Locate every leukocyte (white blood cell).
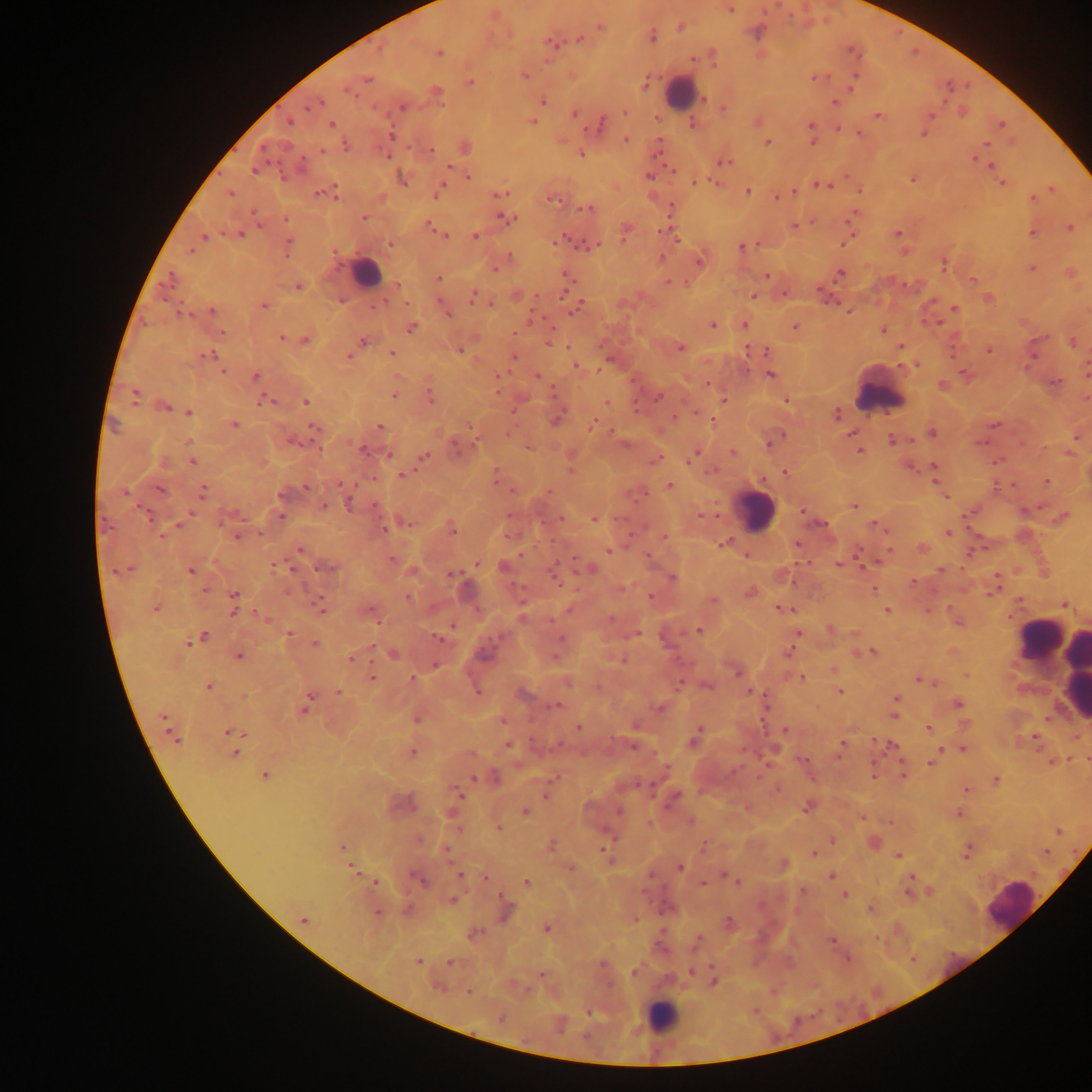
Approximate centers as {x, y} in pixels.
Leukocytes: {681, 92}, {365, 271}, {879, 396}, {756, 511}, {1039, 638}, {1059, 652}, {1074, 674}, {1010, 904}, {663, 1016}.

Summary:
  - Plasmodium parasite locations: {730, 8}, {600, 26}, {681, 26}, {653, 38}, {579, 40}, {550, 42}, {439, 54}, {525, 75}, {817, 77}, {367, 80}, {854, 81}, {471, 82}, {646, 82}, {347, 90}, {437, 92}, {706, 99}, {543, 101}, {315, 103}, {836, 103}, {309, 107}, {402, 107}, {724, 108}, {624, 112}, {574, 114}, {878, 115}, {930, 116}, {532, 122}, {289, 123}, {331, 123}, {694, 124}, {811, 124}, {1001, 124}, {599, 126}, {839, 129}, {859, 134}, {924, 135}, {391, 136}, {626, 139}, {767, 142}, {812, 142}, {986, 144}, {346, 146}, {466, 148}, {322, 150}, {431, 150}, {581, 154}, {388, 156}, {976, 159}, {723, 162}, {302, 163}, {991, 165}, {254, 171}, {468, 177}, {648, 177}, {402, 179}, {913, 179}, {695, 182}, {1002, 183}, {823, 185}, {1052, 189}, {439, 191}, {748, 191}, {321, 192}, {794, 192}, {230, 193}, {330, 193}, {501, 193}, {336, 196}, {777, 197}, {554, 199}, {1033, 199}, {670, 208}, {587, 209}, {364, 218}, {285, 219}, {508, 219}, {431, 226}, {795, 226}, {1070, 228}, {437, 229}, {664, 231}, {239, 233}, {898, 233}, {1032, 233}, {443, 234}, {625, 234}, {475, 236}, {205, 238}, {569, 241}, {846, 241}, {288, 242}, {390, 244}, {594, 244}, {741, 246}, {190, 250}, {509, 256}, {662, 258}, {699, 260}, {944, 264}, {1032, 267}, {841, 273}, {567, 274}, {766, 275}, {171, 278}, {439, 279}, {972, 280}, {669, 282}, {397, 285}, {299, 287}, {472, 295}, {753, 296}, {378, 304}, {491, 305}, {576, 305}, {263, 306}, {955, 308}, {212, 311}, {185, 314}, {447, 314}, {936, 323}, {712, 325}, {744, 326}, {794, 327}, {411, 328}, {884, 330}, {222, 333}, {514, 333}, {281, 337}, {306, 340}, {550, 341}, {364, 342}, {1072, 343}, {681, 347}, {901, 347}, {459, 350}, {748, 350}, {989, 350}, {766, 351}, {393, 353}, {349, 355}, {209, 356}, {513, 357}, {576, 366}, {224, 372}, {1086, 372}, {770, 375}, {255, 376}, {537, 376}, {1056, 382}, {943, 385}, {394, 396}, {431, 396}, {659, 396}, {134, 397}, {724, 400}, {787, 400}, {267, 401}, {306, 402}, {607, 403}, {165, 408}, {189, 412}, {836, 414}, {557, 419}, {709, 420}, {234, 424}, {995, 425}, {592, 426}, {379, 427}, {314, 429}, {932, 432}, {851, 435}, {1075, 437}, {892, 440}, {769, 445}, {363, 451}, {860, 451}, {733, 452}, {388, 455}, {424, 457}, {692, 457}, {656, 460}, {193, 462}, {934, 466}, {911, 467}, {711, 471}, {785, 472}, {403, 475}, {1046, 482}, {342, 484}, {670, 485}, {306, 487}, {160, 490}, {203, 491}, {125, 492}, {281, 495}, {944, 496}, {349, 504}, {323, 506}, {854, 506}, {802, 511}, {192, 512}, {145, 514}, {281, 516}, {561, 518}, {595, 518}, {1062, 518}, {407, 523}, {179, 525}, {876, 525}, {384, 529}, {453, 530}, {948, 532}, {236, 537}, {664, 537}, {722, 543}, {797, 544}, {922, 548}, {300, 549}, {608, 551}, {392, 559}, {838, 564}, {477, 565}, {285, 567}, {327, 567}, {504, 567}, {587, 568}, {941, 570}, {190, 571}, {117, 572}, {453, 574}, {555, 577}, {672, 578}, {205, 591}, {993, 591}, {749, 593}, {234, 594}, {650, 596}, {408, 598}, {713, 600}, {1065, 604}, {155, 608}, {234, 608}, {784, 608}, {570, 609}, {320, 610}, {887, 610}, {371, 611}, {522, 617}, {698, 630}, {289, 634}, {796, 635}, {204, 636}, {437, 637}, {188, 644}, {316, 644}, {871, 652}, {788, 653}, {393, 655}, {554, 655}, {239, 656}, {351, 659}, {621, 660}, {435, 665}, {737, 672}, {966, 675}, {372, 676}, {801, 678}, {413, 679}, {568, 682}, {924, 682}, {680, 684}, {708, 686}, {208, 687}, {750, 691}, {840, 691}, {339, 692}, {524, 695}, {310, 698}, {896, 698}, {958, 704}, {556, 705}, {306, 708}, {660, 708}, {893, 716}, {164, 718}, {416, 720}, {502, 720}, {578, 727}, {928, 729}, {784, 730}, {231, 731}, {698, 732}, {1033, 737}, {693, 740}, {175, 741}, {842, 744}, {508, 745}, {891, 745}, {963, 750}, {412, 752}, {236, 753}, {932, 763}, {264, 776}, {473, 778}, {996, 780}, {966, 790}, {459, 793}, {546, 796}, {674, 797}, {807, 808}, {619, 811}, {525, 812}, {691, 821}, {499, 828}, {419, 839}, {551, 845}, {343, 847}, {606, 849}, {447, 852}, {814, 853}, {899, 854}, {680, 867}, {352, 868}, {460, 874}, {729, 877}, {831, 877}, {911, 877}, {485, 878}, {420, 880}, {735, 880}, {526, 881}, {375, 882}, {908, 893}, {845, 895}, {453, 901}, {871, 908}, {377, 913}, {303, 920}, {729, 922}, {546, 928}, {475, 933}, {832, 941}, {417, 962}, {450, 962}, {691, 972}, {634, 973}, {714, 981}, {437, 987}, {469, 991}, {501, 1017}
  - Country: Ghana
  - Field of view: single
  - Preparation: thick blood smear
  - Image size: 1092×1092 pixels
  - Capture: mobile-phone photograph through a microscope